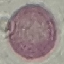
malaria status = uninfected
image type = cell patch, automatically extracted from a larger field of view and resized to 64 × 64 pixels
stain = Giemsa
preparation = thin blood film
capture = smartphone camera at the microscope eyepiece